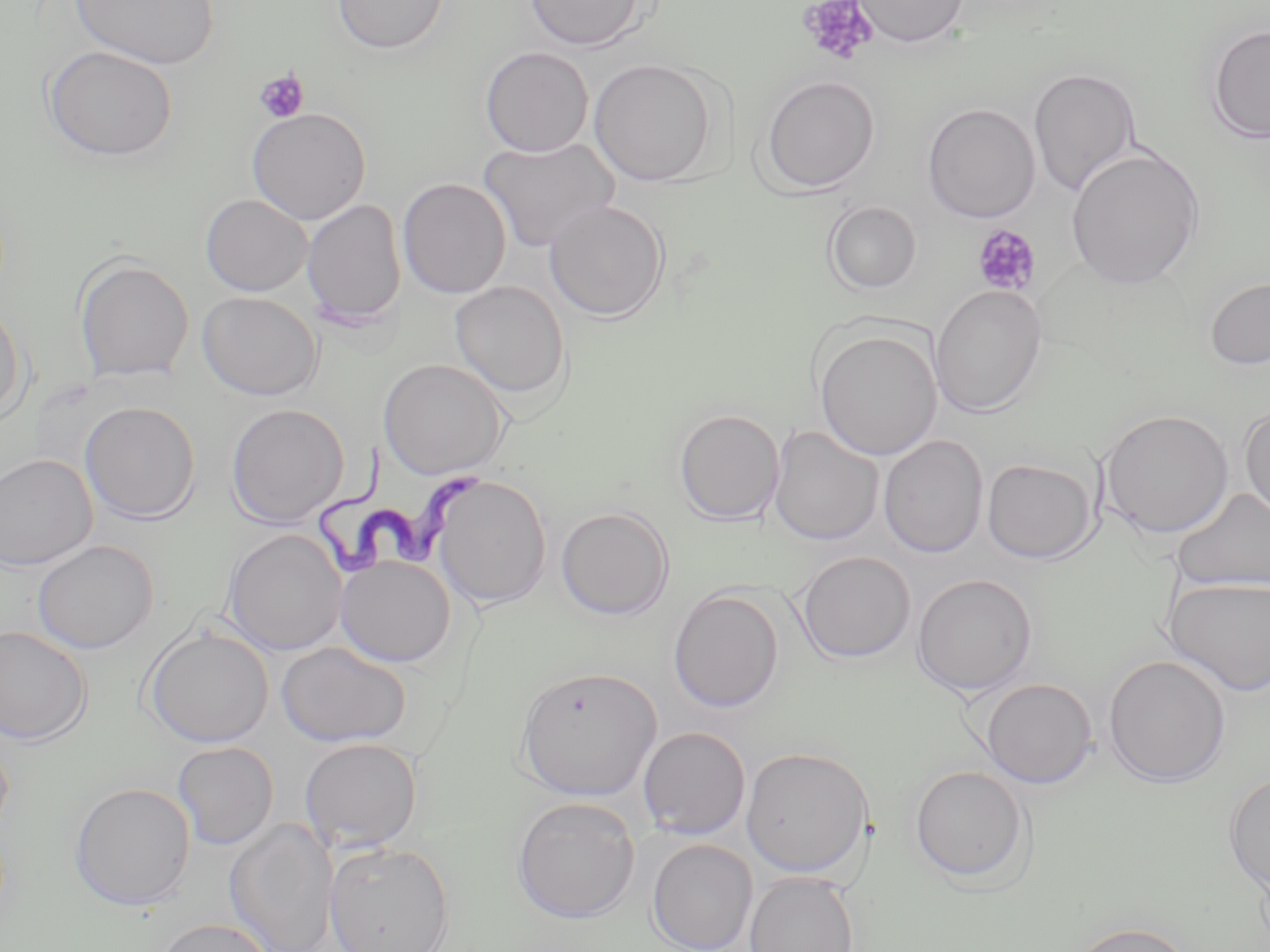

Summary:
  - Coordinate format: approximate bounding boxes as (x1, y1, x2, y2) in pixels
  - Uninfected red blood cell locations: (71, 0, 219, 69), (332, 0, 449, 54), (524, 0, 647, 51), (852, 0, 969, 48), (1206, 22, 1270, 145), (42, 45, 179, 162), (479, 46, 593, 158), (588, 58, 720, 186), (1028, 67, 1141, 196), (759, 74, 881, 195), (924, 104, 1044, 225), (247, 107, 371, 225), (478, 136, 619, 252), (1065, 147, 1204, 290), (397, 178, 512, 299), (201, 194, 313, 296), (302, 198, 406, 328), (544, 200, 670, 322), (823, 200, 923, 296), (73, 256, 194, 383), (1204, 277, 1270, 370), (448, 280, 570, 401), (929, 283, 1046, 418), (197, 291, 323, 400), (0, 301, 28, 423), (813, 327, 942, 460), (378, 358, 509, 480), (80, 401, 201, 523), (226, 403, 349, 527), (1239, 404, 1270, 524), (673, 408, 785, 525), (1100, 409, 1234, 538), (768, 425, 884, 546), (877, 435, 989, 558), (0, 454, 98, 571), (981, 457, 1098, 564), (432, 475, 552, 610), (1171, 487, 1270, 593), (555, 506, 674, 621), (223, 528, 347, 656), (32, 539, 159, 654), (796, 551, 916, 664), (336, 554, 456, 667), (912, 573, 1037, 697), (1161, 576, 1270, 697), (667, 588, 785, 712), (0, 625, 92, 745), (143, 625, 273, 748), (277, 641, 412, 748), (1103, 654, 1232, 789), (515, 665, 663, 801), (980, 678, 1097, 788), (637, 726, 751, 839), (0, 734, 14, 840), (299, 737, 423, 853), (172, 741, 279, 850), (741, 745, 875, 878), (909, 764, 1032, 884), (1223, 773, 1270, 891), (69, 781, 196, 911), (511, 796, 641, 924), (225, 819, 338, 952), (647, 839, 758, 952), (323, 840, 455, 952), (744, 871, 861, 952), (154, 917, 274, 952), (1065, 920, 1196, 952)
  - Platelet locations: (797, 0, 880, 66), (254, 69, 309, 123), (971, 224, 1041, 297)
  - Trypanosoma brucei locations: (314, 444, 492, 577)
  - Slide-level diagnosis: Trypanosoma brucei
  - Preparation: thin blood film
  - Field of view: single
  - Magnification: 1000x
  - Modality: light microscopy
  - Stain: May-Grünwald-Giemsa
  - Image size: 1270×952 pixels